Assess the morphology of the red blood cells.
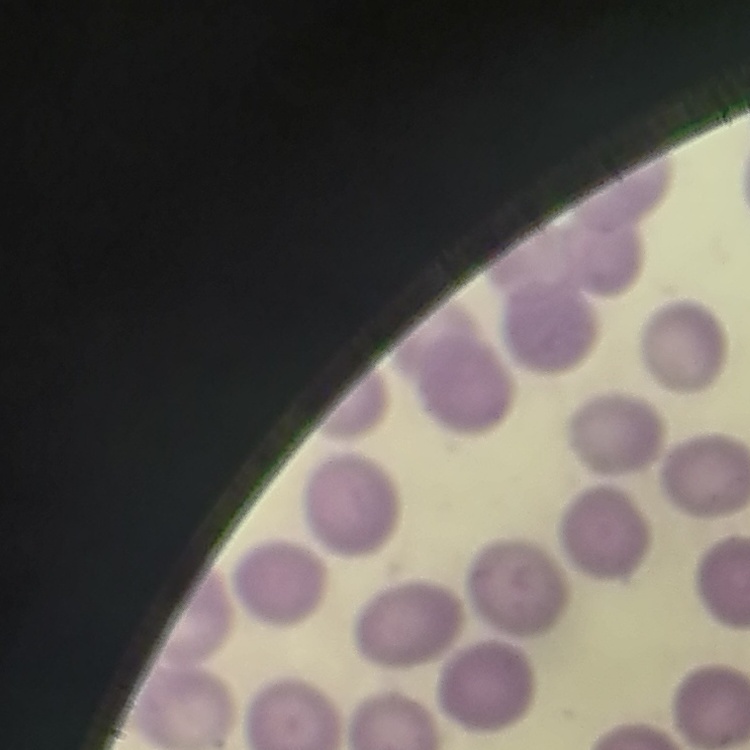

They show no rouleaux formation.

Thin blood film. Stained with either Field's or Giemsa. One tile cut from a larger photomicrograph.